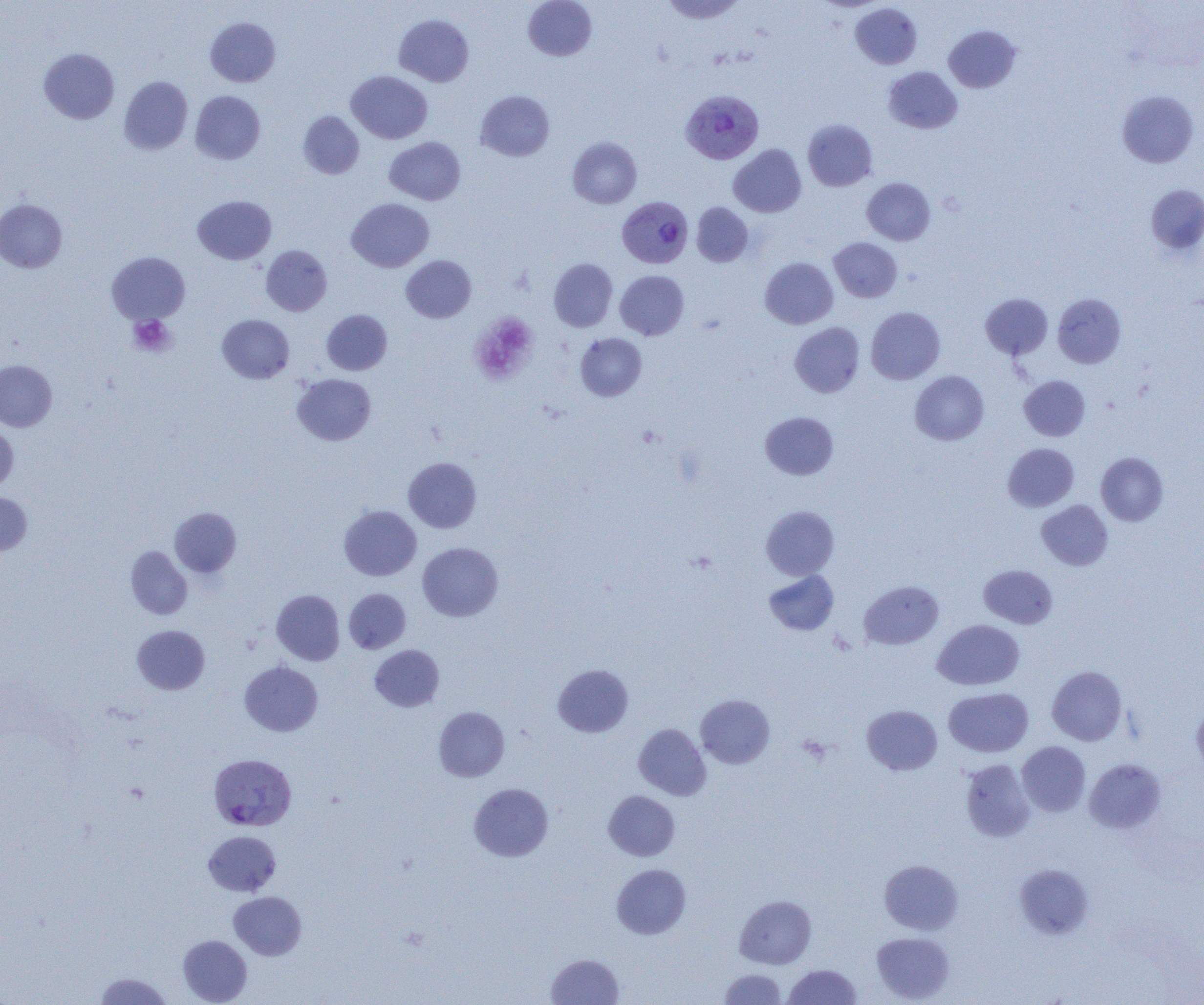 Approximate bounding boxes as named x1/y1/x2/y2 corners in pixels. Uninfected red blood cell locations: (x1=523, y1=0, x2=597, y2=61), (x1=659, y1=0, x2=747, y2=24), (x1=850, y1=3, x2=922, y2=69), (x1=394, y1=14, x2=474, y2=87), (x1=205, y1=17, x2=281, y2=87), (x1=943, y1=25, x2=1021, y2=92), (x1=39, y1=48, x2=120, y2=124), (x1=883, y1=66, x2=962, y2=134), (x1=346, y1=70, x2=432, y2=144), (x1=119, y1=76, x2=193, y2=155), (x1=475, y1=90, x2=554, y2=161), (x1=1116, y1=90, x2=1199, y2=168), (x1=190, y1=91, x2=266, y2=164), (x1=298, y1=111, x2=364, y2=179), (x1=802, y1=119, x2=877, y2=191), (x1=384, y1=137, x2=465, y2=205), (x1=568, y1=137, x2=642, y2=209), (x1=728, y1=144, x2=807, y2=217), (x1=861, y1=178, x2=935, y2=245), (x1=1145, y1=184, x2=1204, y2=258), (x1=192, y1=195, x2=276, y2=264), (x1=347, y1=198, x2=434, y2=272), (x1=0, y1=199, x2=67, y2=272), (x1=691, y1=202, x2=753, y2=266), (x1=829, y1=237, x2=902, y2=302), (x1=261, y1=245, x2=332, y2=316), (x1=106, y1=252, x2=189, y2=324), (x1=401, y1=255, x2=476, y2=322), (x1=760, y1=257, x2=838, y2=329), (x1=549, y1=258, x2=618, y2=331), (x1=615, y1=270, x2=689, y2=340), (x1=981, y1=293, x2=1053, y2=359), (x1=1052, y1=293, x2=1126, y2=368), (x1=866, y1=306, x2=945, y2=384), (x1=321, y1=309, x2=392, y2=375), (x1=217, y1=314, x2=294, y2=383), (x1=790, y1=322, x2=865, y2=398), (x1=575, y1=333, x2=647, y2=401), (x1=0, y1=359, x2=57, y2=431), (x1=910, y1=370, x2=989, y2=445), (x1=293, y1=374, x2=376, y2=445), (x1=1019, y1=375, x2=1090, y2=441), (x1=760, y1=411, x2=839, y2=480), (x1=0, y1=425, x2=18, y2=494), (x1=1003, y1=443, x2=1079, y2=512), (x1=1096, y1=452, x2=1169, y2=526), (x1=403, y1=456, x2=482, y2=533), (x1=0, y1=493, x2=32, y2=555), (x1=1037, y1=500, x2=1113, y2=570), (x1=339, y1=505, x2=421, y2=581), (x1=761, y1=506, x2=839, y2=580), (x1=169, y1=507, x2=241, y2=578), (x1=418, y1=542, x2=503, y2=621), (x1=126, y1=546, x2=192, y2=619), (x1=978, y1=565, x2=1057, y2=628), (x1=763, y1=570, x2=839, y2=636), (x1=858, y1=580, x2=944, y2=649), (x1=343, y1=588, x2=411, y2=654), (x1=272, y1=589, x2=344, y2=665), (x1=932, y1=619, x2=1024, y2=690), (x1=132, y1=625, x2=210, y2=694), (x1=369, y1=645, x2=444, y2=712), (x1=239, y1=661, x2=323, y2=736), (x1=552, y1=664, x2=634, y2=737), (x1=1047, y1=665, x2=1128, y2=745), (x1=943, y1=687, x2=1034, y2=757), (x1=696, y1=694, x2=775, y2=769), (x1=1192, y1=703, x2=1204, y2=773), (x1=862, y1=705, x2=942, y2=775), (x1=433, y1=706, x2=509, y2=782), (x1=633, y1=723, x2=711, y2=800), (x1=1017, y1=741, x2=1090, y2=816), (x1=1084, y1=758, x2=1166, y2=834), (x1=960, y1=759, x2=1035, y2=842), (x1=468, y1=783, x2=554, y2=862), (x1=603, y1=790, x2=680, y2=861), (x1=203, y1=830, x2=281, y2=895), (x1=879, y1=859, x2=963, y2=934), (x1=611, y1=863, x2=691, y2=939), (x1=1014, y1=864, x2=1094, y2=939), (x1=229, y1=891, x2=306, y2=960), (x1=734, y1=895, x2=816, y2=969), (x1=871, y1=932, x2=954, y2=1003), (x1=177, y1=935, x2=252, y2=1005), (x1=546, y1=953, x2=624, y2=1004), (x1=783, y1=964, x2=861, y2=1005), (x1=718, y1=969, x2=787, y2=1004), (x1=93, y1=972, x2=173, y2=1004). Plasmodium vivax-infected red blood cell locations: (x1=680, y1=89, x2=764, y2=165), (x1=614, y1=198, x2=690, y2=269), (x1=208, y1=754, x2=296, y2=831). Platelet locations: (x1=469, y1=313, x2=538, y2=385), (x1=128, y1=315, x2=176, y2=357). Slide-level diagnosis: Plasmodium vivax. Single field of view. Thin blood film. Light microscopy. Image is 1204×1005 pixels. 1000x magnification.